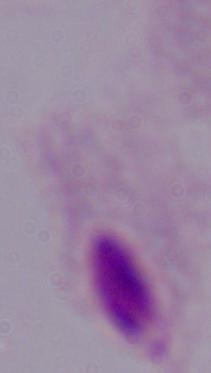
identification = trichomonad
magnification = 1000x
modality = photomicrograph